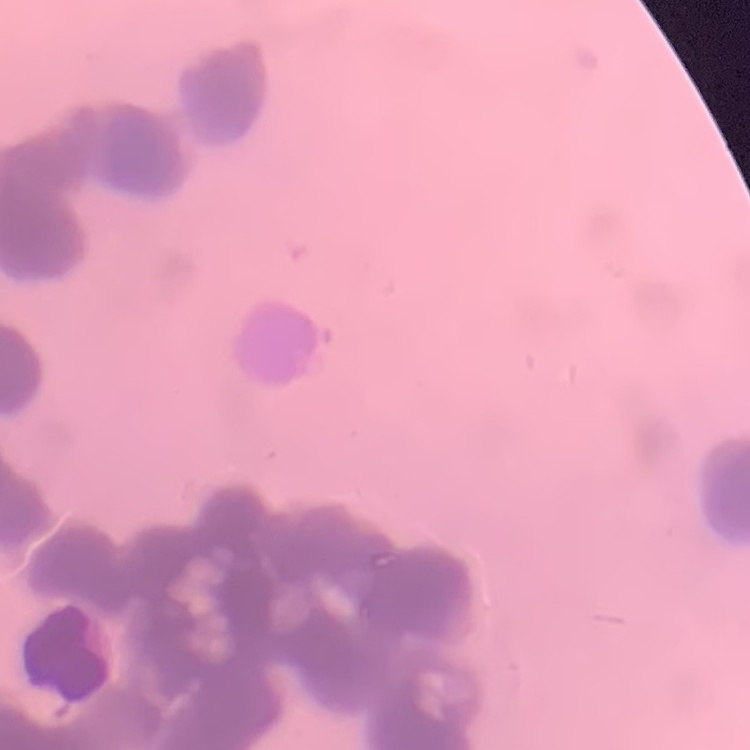

Summary:
  - Red blood cell morphology: rouleaux formation
  - Preparation: thin blood film
  - Image type: one tile cut from a larger photomicrograph
  - Stain: Field's or Giemsa